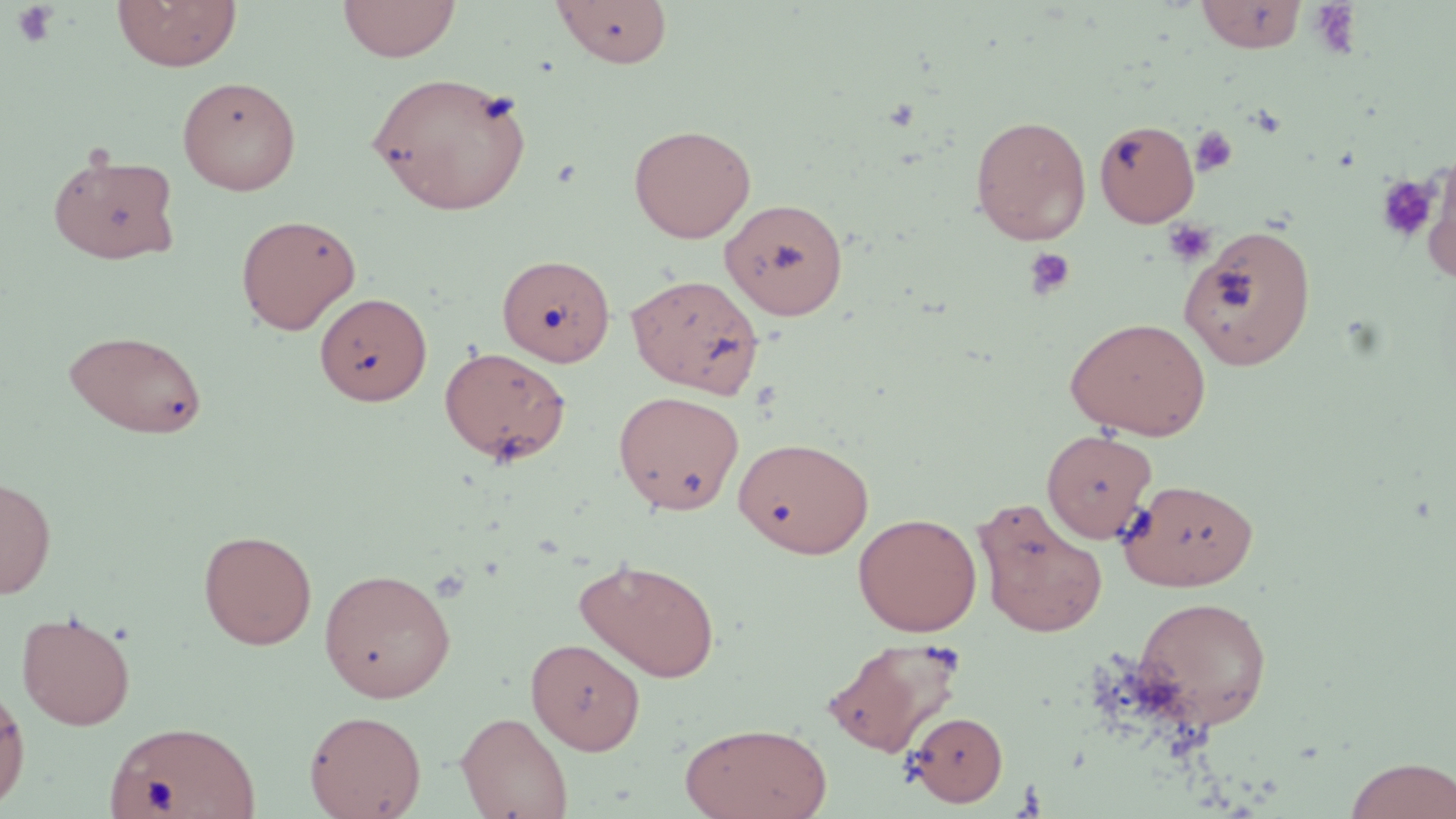
slide-level diagnosis = no evidence of blood parasites
platelet locations = approximate bounding boxes as (x1,y1)-(x2,y2) corner pairs in pixels: (1307,1)-(1364,58), (12,2)-(59,49), (1191,127)-(1237,176), (1375,174)-(1441,244), (1163,219)-(1217,266), (1024,247)-(1075,300)
stain = May-Grünwald-Giemsa
magnification = 1000x
image size = 1456×819 pixels
field of view = one of a larger specimen
modality = light microscopy
preparation = thin blood film
uninfected red blood cell locations = approximate bounding boxes as (x1,y1)-(x2,y2) corner pairs in pixels: (111,0)-(242,72), (338,0)-(460,62), (552,0)-(673,68), (1195,0)-(1308,53), (367,71)-(529,216), (177,76)-(301,195), (970,114)-(1091,245), (1094,121)-(1200,227), (629,124)-(756,243), (48,152)-(181,265), (1422,152)-(1456,283), (720,198)-(848,320), (235,213)-(361,335), (1180,224)-(1317,371), (496,259)-(615,372), (626,272)-(765,397), (314,292)-(432,405), (1064,316)-(1212,440), (63,329)-(209,439), (439,346)-(571,465), (613,389)-(744,514), (1042,428)-(1157,542), (733,436)-(874,558), (0,475)-(56,598), (1120,478)-(1260,590), (973,498)-(1109,638), (853,512)-(982,636), (198,529)-(318,650), (575,558)-(720,683), (318,567)-(456,702), (1133,595)-(1273,730), (16,610)-(136,729), (526,637)-(645,754), (823,637)-(966,758), (0,681)-(30,812), (304,709)-(427,819), (455,711)-(573,819), (907,711)-(1009,807), (104,719)-(259,819), (680,721)-(833,819), (1344,756)-(1456,818)